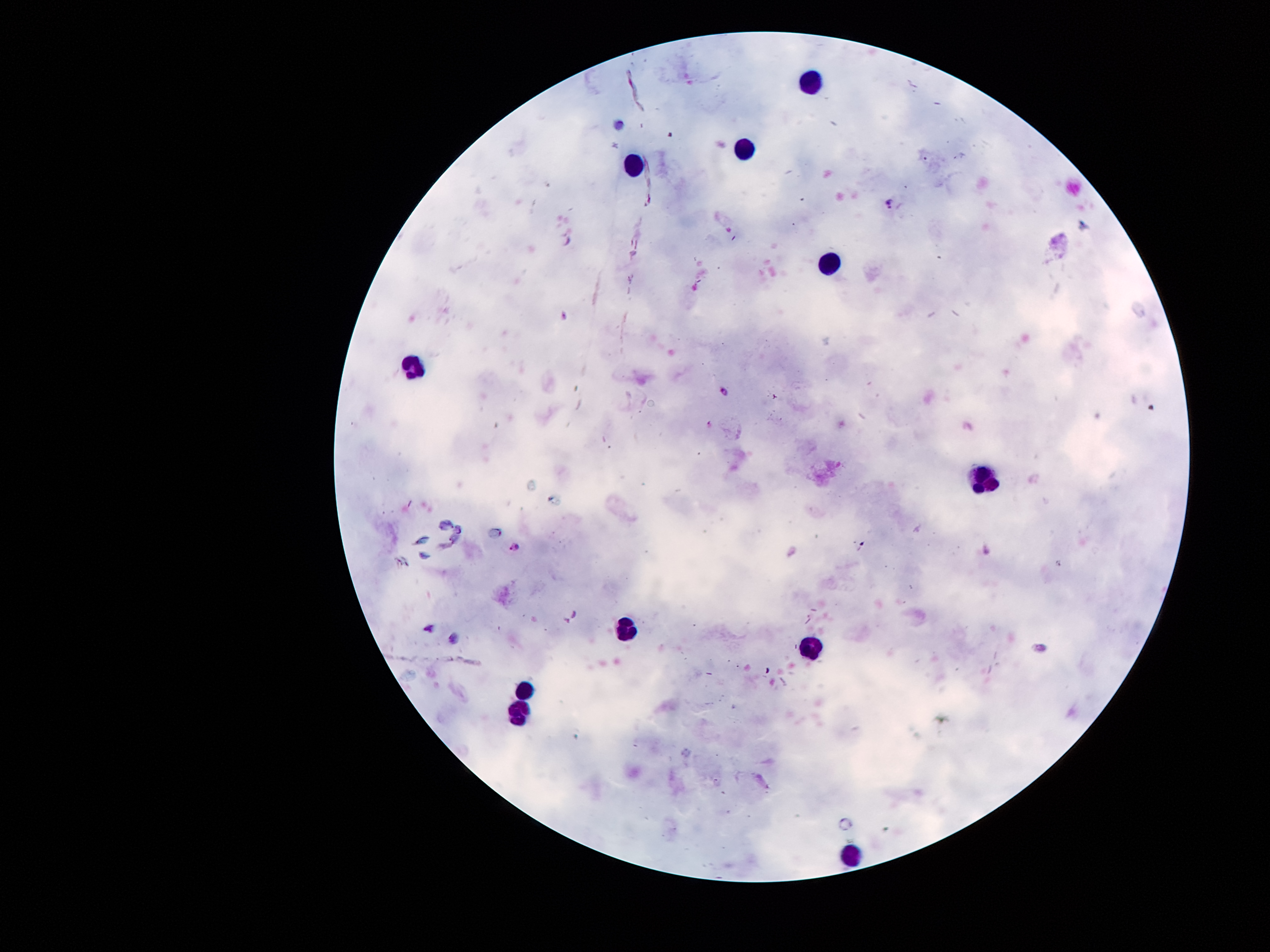
Approximate centers as (x, y) in pixels.
Summary:
  - Leukocyte locations: (811, 79), (745, 150), (632, 164), (833, 259), (413, 368), (983, 481), (628, 627), (807, 650), (522, 694), (515, 714), (847, 853)
  - Plasmodium parasite locations: (891, 205), (563, 315), (724, 393), (516, 545)
  - Preparation: thick blood film
  - Stain: Giemsa
  - Magnification: 100x
  - Field of view: one from this slide
  - Patient malaria status: positive for Plasmodium falciparum
  - Image size: 1270×952 pixels
  - Capture: smartphone through the microscope eyepiece